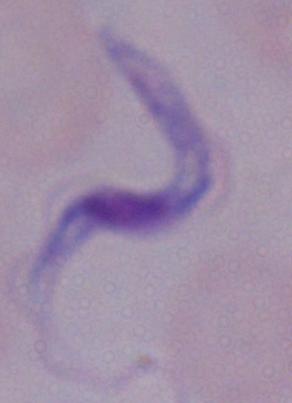
Micrograph. A trypanosome is seen. Captured at 1000x magnification.